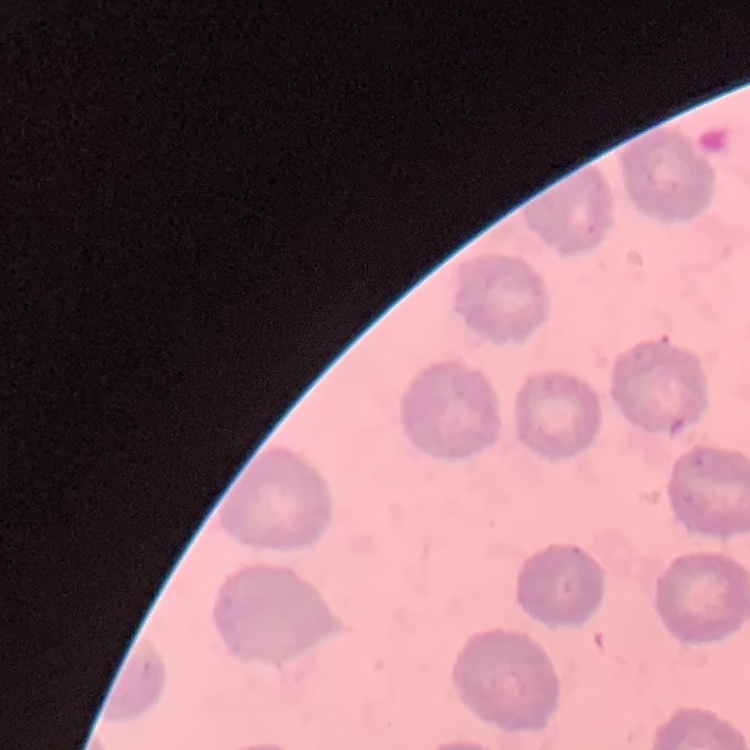

Summary:
  - Red blood cell morphology: no rouleaux formation
  - Image type: one tile cut from a larger photomicrograph
  - Stain: Field's or Giemsa
  - Preparation: thin blood film